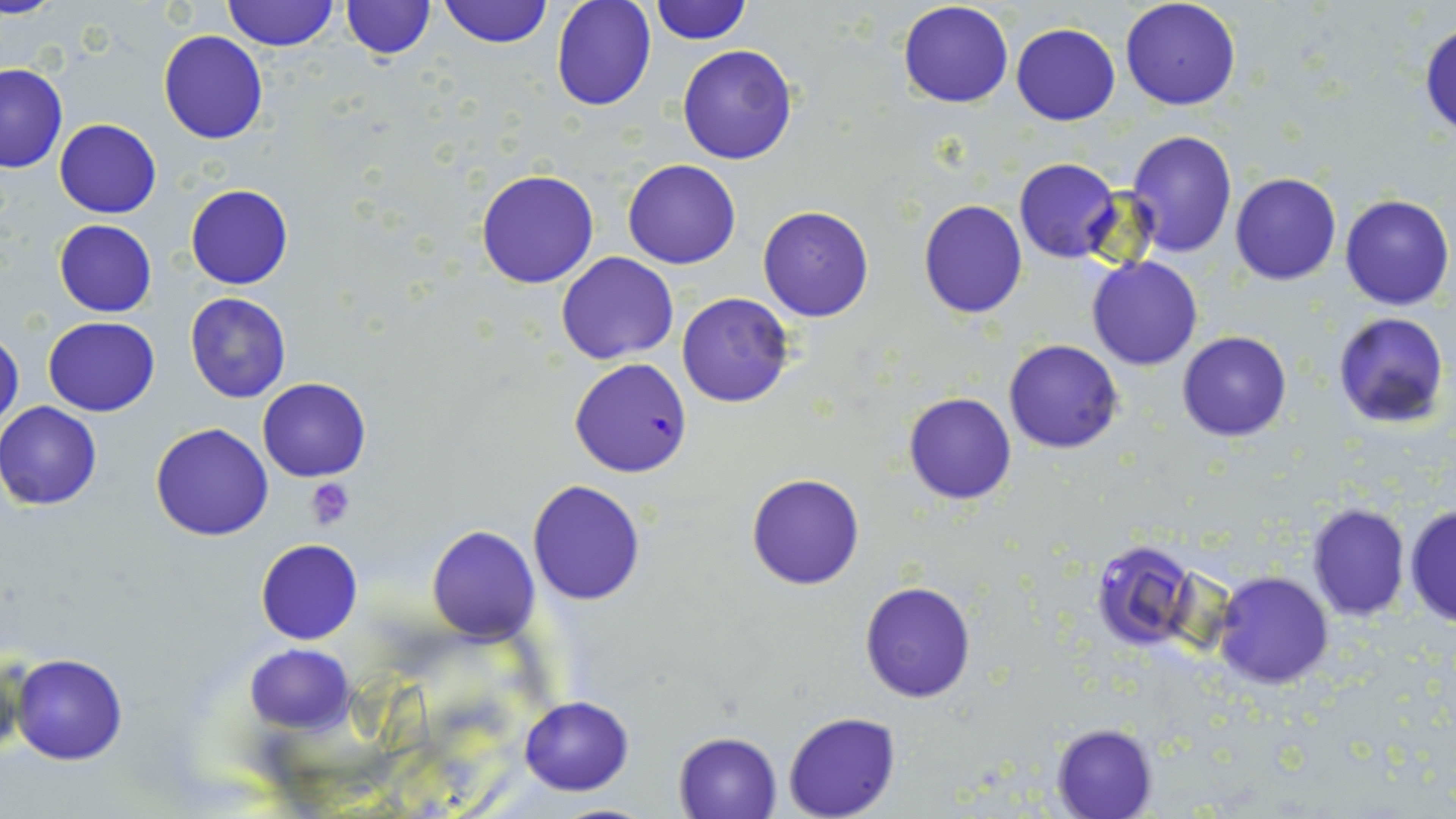 Approximate bounding boxes as (x1, y1, x2, y2) in pixels. Platelet locations: (306, 478, 356, 528). Uninfected red blood cell locations: (0, 0, 58, 18), (222, 0, 337, 51), (437, 0, 551, 49), (551, 0, 657, 112), (648, 0, 753, 45), (897, 0, 1014, 108), (1120, 0, 1242, 111), (338, 1, 435, 59), (1011, 22, 1120, 124), (1420, 22, 1456, 140), (159, 31, 269, 144), (676, 44, 798, 164), (0, 62, 67, 172), (55, 118, 161, 218), (1126, 130, 1237, 256), (1014, 158, 1122, 262), (624, 159, 741, 268), (476, 169, 600, 289), (1229, 173, 1342, 286), (185, 184, 294, 290), (1227, 187, 1453, 300), (1339, 194, 1454, 310), (919, 200, 1027, 319), (758, 205, 873, 321), (53, 219, 157, 317), (556, 252, 679, 365), (1086, 256, 1204, 371), (184, 292, 291, 403), (676, 294, 795, 408), (1331, 311, 1450, 430), (44, 317, 161, 416), (0, 329, 23, 437), (1176, 331, 1292, 442), (1003, 340, 1124, 453), (258, 378, 370, 482), (903, 391, 1017, 504), (0, 402, 103, 510), (151, 422, 273, 541), (746, 473, 865, 591), (528, 479, 646, 605), (1306, 502, 1411, 622), (1405, 503, 1455, 631), (427, 525, 539, 644), (1090, 538, 1204, 648), (255, 539, 363, 644), (1212, 572, 1334, 689), (859, 582, 976, 702), (245, 643, 355, 733), (11, 653, 127, 765), (518, 695, 635, 796), (782, 712, 901, 819), (1051, 722, 1159, 818), (673, 732, 781, 818). Plasmodium falciparum-infected red blood cell locations: (569, 358, 692, 478). Slide-level diagnosis: Plasmodium falciparum. Captured at 1000x magnification. Single field of view. Thin blood smear. Light microscopy. May-Grünwald-Giemsa-stained preparation. Image is 1456×819 pixels.